Name the cell type shown.
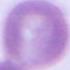

This is an erythrocyte.

Captured at 1000x magnification. Photomicrograph.